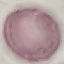

malaria_status: uninfected
stain: Giemsa
capture: smartphone camera at the microscope eyepiece
image_type: cell patch, automatically extracted from a larger field of view and resized to 64 × 64 pixels
preparation: thin smear